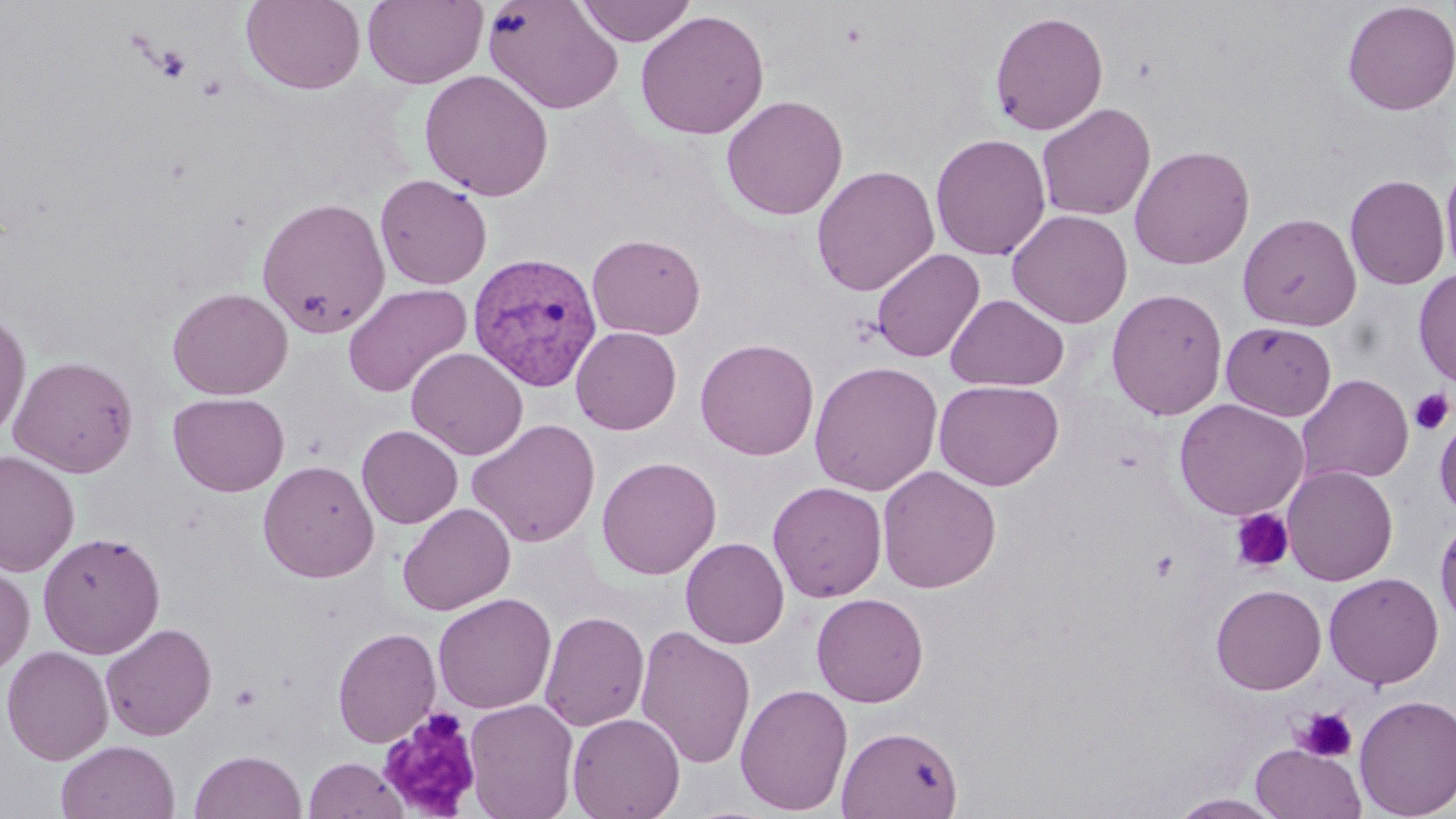

Approximate bounding boxes as named x1/y1/x2/y2 corners in pixels. Platelet locations: (x1=153, y1=45, x2=192, y2=82), (x1=1409, y1=388, x2=1454, y2=435), (x1=1230, y1=509, x2=1295, y2=573), (x1=1150, y1=549, x2=1181, y2=582), (x1=1293, y1=707, x2=1358, y2=763), (x1=376, y1=708, x2=483, y2=818). Uninfected red blood cell locations: (x1=241, y1=0, x2=366, y2=94), (x1=362, y1=0, x2=488, y2=88), (x1=483, y1=0, x2=624, y2=114), (x1=576, y1=0, x2=696, y2=46), (x1=1341, y1=0, x2=1456, y2=116), (x1=635, y1=9, x2=769, y2=140), (x1=989, y1=10, x2=1109, y2=136), (x1=419, y1=69, x2=554, y2=201), (x1=721, y1=95, x2=848, y2=220), (x1=1036, y1=102, x2=1156, y2=221), (x1=930, y1=133, x2=1051, y2=260), (x1=1129, y1=144, x2=1255, y2=270), (x1=1440, y1=160, x2=1456, y2=281), (x1=811, y1=165, x2=939, y2=296), (x1=375, y1=174, x2=492, y2=289), (x1=1344, y1=174, x2=1450, y2=290), (x1=256, y1=196, x2=391, y2=338), (x1=1007, y1=209, x2=1133, y2=328), (x1=1237, y1=212, x2=1361, y2=331), (x1=587, y1=233, x2=706, y2=340), (x1=871, y1=248, x2=985, y2=363), (x1=1413, y1=268, x2=1456, y2=388), (x1=342, y1=283, x2=472, y2=398), (x1=167, y1=287, x2=293, y2=400), (x1=1106, y1=287, x2=1228, y2=420), (x1=945, y1=294, x2=1069, y2=391), (x1=0, y1=308, x2=31, y2=439), (x1=1221, y1=321, x2=1336, y2=421), (x1=571, y1=326, x2=682, y2=435), (x1=695, y1=337, x2=819, y2=460), (x1=406, y1=347, x2=528, y2=461), (x1=7, y1=355, x2=139, y2=477), (x1=809, y1=360, x2=943, y2=496), (x1=1296, y1=373, x2=1414, y2=485), (x1=933, y1=379, x2=1064, y2=491), (x1=168, y1=392, x2=289, y2=497), (x1=1173, y1=398, x2=1309, y2=520), (x1=1434, y1=413, x2=1456, y2=520), (x1=466, y1=418, x2=601, y2=548), (x1=357, y1=424, x2=463, y2=529), (x1=0, y1=450, x2=79, y2=578), (x1=596, y1=456, x2=721, y2=580), (x1=258, y1=460, x2=379, y2=583), (x1=877, y1=465, x2=1001, y2=593), (x1=1282, y1=465, x2=1398, y2=586), (x1=768, y1=481, x2=887, y2=602), (x1=397, y1=502, x2=516, y2=616), (x1=1435, y1=515, x2=1456, y2=633), (x1=37, y1=531, x2=166, y2=658), (x1=680, y1=537, x2=789, y2=648), (x1=0, y1=567, x2=35, y2=676), (x1=1323, y1=572, x2=1444, y2=689), (x1=1211, y1=583, x2=1327, y2=695), (x1=432, y1=593, x2=556, y2=715), (x1=811, y1=593, x2=929, y2=707), (x1=540, y1=611, x2=649, y2=732), (x1=100, y1=622, x2=217, y2=741), (x1=635, y1=625, x2=756, y2=769), (x1=332, y1=626, x2=441, y2=748), (x1=1, y1=645, x2=114, y2=765), (x1=735, y1=683, x2=853, y2=815), (x1=1353, y1=694, x2=1455, y2=818), (x1=463, y1=698, x2=579, y2=818), (x1=567, y1=712, x2=685, y2=819), (x1=837, y1=725, x2=964, y2=819), (x1=56, y1=739, x2=180, y2=819), (x1=1251, y1=744, x2=1366, y2=819), (x1=189, y1=750, x2=307, y2=819), (x1=303, y1=757, x2=407, y2=818), (x1=1169, y1=793, x2=1286, y2=818). Plasmodium vivax-infected red blood cell locations: (x1=467, y1=251, x2=603, y2=391). Slide-level diagnosis: Plasmodium vivax. Optical microscopy. Image is 1456×819 pixels. Single field of view. Thin blood smear. Captured at 1000x magnification. May-Grünwald-Giemsa stain.